Describe the morphology of the red blood cells.
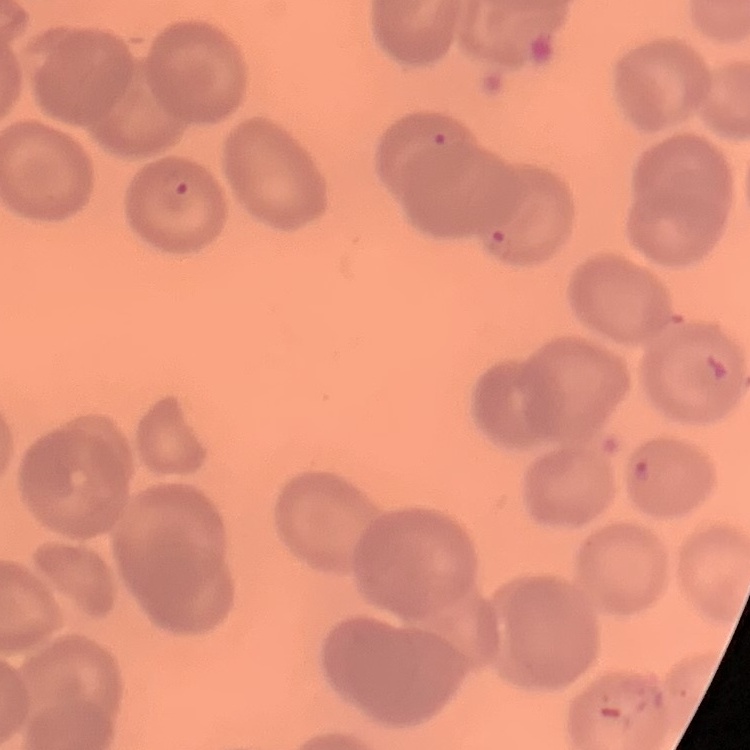

No rouleaux formation.

stain = Field's or Giemsa
image type = square crop of a larger photomicrograph
preparation = thin blood smear